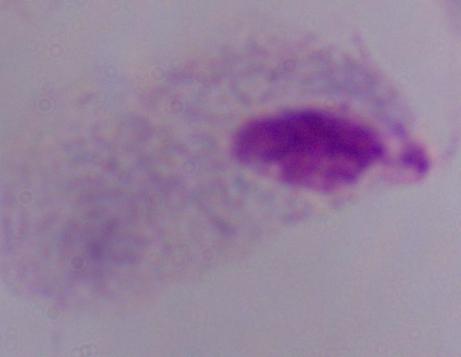
Captured at 1000x magnification. A trichomonad is shown. Photomicrograph.